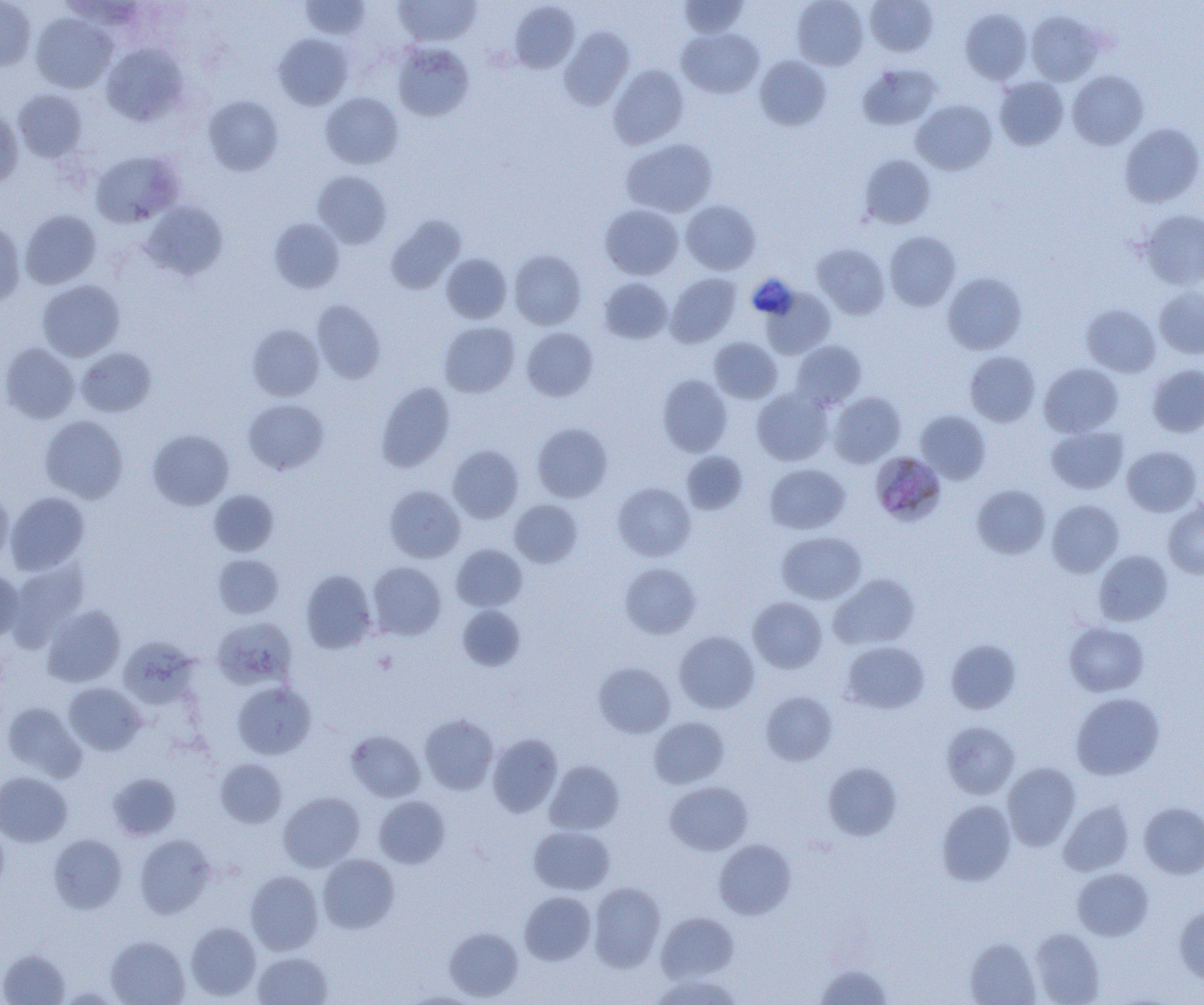
Summary:
  - Coordinate format: approximate bounding boxes as named x1/y1/x2/y2 corners in pixels
  - Uninfected red blood cell locations: (x1=299, y1=0, x2=371, y2=40), (x1=393, y1=0, x2=481, y2=46), (x1=792, y1=0, x2=868, y2=70), (x1=866, y1=0, x2=938, y2=56), (x1=0, y1=1, x2=36, y2=71), (x1=679, y1=1, x2=748, y2=38), (x1=509, y1=2, x2=580, y2=73), (x1=961, y1=8, x2=1032, y2=84), (x1=1025, y1=11, x2=1103, y2=85), (x1=31, y1=13, x2=116, y2=93), (x1=559, y1=27, x2=634, y2=110), (x1=677, y1=28, x2=764, y2=98), (x1=273, y1=33, x2=354, y2=110), (x1=392, y1=42, x2=474, y2=120), (x1=101, y1=44, x2=188, y2=126), (x1=754, y1=55, x2=831, y2=131), (x1=857, y1=63, x2=942, y2=130), (x1=608, y1=64, x2=688, y2=149), (x1=1067, y1=70, x2=1149, y2=149), (x1=994, y1=77, x2=1068, y2=150), (x1=13, y1=90, x2=88, y2=162), (x1=320, y1=92, x2=404, y2=169), (x1=203, y1=95, x2=283, y2=175), (x1=912, y1=99, x2=997, y2=175), (x1=0, y1=109, x2=23, y2=189), (x1=1119, y1=122, x2=1204, y2=207), (x1=622, y1=138, x2=717, y2=217), (x1=90, y1=150, x2=184, y2=227), (x1=859, y1=154, x2=936, y2=229), (x1=313, y1=170, x2=392, y2=248), (x1=681, y1=199, x2=760, y2=274), (x1=142, y1=200, x2=227, y2=280), (x1=600, y1=204, x2=683, y2=279), (x1=20, y1=210, x2=101, y2=289), (x1=1140, y1=210, x2=1204, y2=289), (x1=385, y1=215, x2=465, y2=294), (x1=269, y1=218, x2=344, y2=293), (x1=0, y1=219, x2=26, y2=307), (x1=884, y1=231, x2=961, y2=311), (x1=812, y1=243, x2=890, y2=319), (x1=509, y1=249, x2=586, y2=330), (x1=441, y1=254, x2=512, y2=324), (x1=942, y1=272, x2=1026, y2=354), (x1=665, y1=273, x2=741, y2=347), (x1=598, y1=278, x2=672, y2=344), (x1=37, y1=279, x2=125, y2=361), (x1=762, y1=287, x2=835, y2=359), (x1=1154, y1=287, x2=1204, y2=359), (x1=311, y1=300, x2=386, y2=383), (x1=1081, y1=303, x2=1160, y2=376), (x1=439, y1=321, x2=520, y2=397), (x1=247, y1=324, x2=324, y2=401), (x1=522, y1=328, x2=598, y2=400), (x1=709, y1=337, x2=782, y2=403), (x1=791, y1=340, x2=867, y2=410), (x1=0, y1=343, x2=80, y2=423), (x1=76, y1=347, x2=156, y2=417), (x1=965, y1=351, x2=1040, y2=426), (x1=1039, y1=363, x2=1123, y2=438), (x1=1146, y1=365, x2=1204, y2=437), (x1=656, y1=374, x2=733, y2=457), (x1=376, y1=382, x2=455, y2=472), (x1=752, y1=388, x2=833, y2=465), (x1=828, y1=392, x2=906, y2=468), (x1=243, y1=398, x2=329, y2=474), (x1=915, y1=410, x2=991, y2=485), (x1=39, y1=415, x2=128, y2=503), (x1=532, y1=422, x2=613, y2=502), (x1=1046, y1=426, x2=1128, y2=494), (x1=147, y1=428, x2=234, y2=510), (x1=448, y1=444, x2=524, y2=523), (x1=1121, y1=445, x2=1202, y2=516), (x1=681, y1=451, x2=748, y2=514), (x1=764, y1=464, x2=850, y2=534), (x1=612, y1=482, x2=696, y2=561), (x1=972, y1=484, x2=1050, y2=559), (x1=384, y1=486, x2=465, y2=563), (x1=0, y1=487, x2=13, y2=570), (x1=208, y1=489, x2=279, y2=556), (x1=5, y1=491, x2=89, y2=575), (x1=510, y1=499, x2=582, y2=568), (x1=1163, y1=499, x2=1204, y2=578), (x1=1046, y1=500, x2=1124, y2=577), (x1=777, y1=531, x2=867, y2=604), (x1=451, y1=544, x2=527, y2=611), (x1=1093, y1=550, x2=1173, y2=626), (x1=212, y1=554, x2=284, y2=619), (x1=7, y1=560, x2=90, y2=648), (x1=367, y1=562, x2=446, y2=640), (x1=619, y1=562, x2=701, y2=639), (x1=0, y1=569, x2=23, y2=644), (x1=300, y1=569, x2=377, y2=653), (x1=829, y1=573, x2=921, y2=650), (x1=748, y1=596, x2=827, y2=672), (x1=42, y1=604, x2=125, y2=687), (x1=457, y1=605, x2=525, y2=671), (x1=211, y1=617, x2=296, y2=690), (x1=1064, y1=622, x2=1149, y2=696), (x1=674, y1=631, x2=759, y2=714), (x1=120, y1=637, x2=200, y2=709), (x1=946, y1=639, x2=1021, y2=714), (x1=841, y1=641, x2=929, y2=713), (x1=594, y1=662, x2=675, y2=738), (x1=233, y1=682, x2=316, y2=759), (x1=63, y1=683, x2=146, y2=755), (x1=761, y1=691, x2=837, y2=765), (x1=1071, y1=692, x2=1165, y2=779), (x1=2, y1=702, x2=85, y2=781), (x1=420, y1=714, x2=498, y2=795), (x1=649, y1=717, x2=729, y2=788), (x1=942, y1=722, x2=1020, y2=798), (x1=346, y1=730, x2=426, y2=802), (x1=487, y1=733, x2=562, y2=817), (x1=215, y1=758, x2=287, y2=827), (x1=544, y1=760, x2=624, y2=834), (x1=823, y1=762, x2=903, y2=841), (x1=1002, y1=762, x2=1081, y2=851), (x1=0, y1=771, x2=72, y2=846), (x1=107, y1=773, x2=181, y2=840), (x1=665, y1=781, x2=753, y2=855), (x1=279, y1=791, x2=365, y2=871), (x1=373, y1=796, x2=450, y2=868), (x1=936, y1=800, x2=1016, y2=886), (x1=1058, y1=801, x2=1134, y2=876), (x1=1139, y1=802, x2=1204, y2=878), (x1=529, y1=826, x2=615, y2=895), (x1=49, y1=833, x2=126, y2=914), (x1=134, y1=834, x2=216, y2=918), (x1=714, y1=839, x2=796, y2=919), (x1=318, y1=854, x2=400, y2=933), (x1=1072, y1=868, x2=1153, y2=940), (x1=245, y1=870, x2=323, y2=955), (x1=588, y1=882, x2=665, y2=972), (x1=520, y1=891, x2=596, y2=965), (x1=1174, y1=905, x2=1204, y2=985), (x1=656, y1=912, x2=739, y2=982), (x1=185, y1=922, x2=261, y2=1001), (x1=444, y1=927, x2=523, y2=1002), (x1=1030, y1=928, x2=1105, y2=1005), (x1=106, y1=936, x2=189, y2=1005), (x1=965, y1=937, x2=1040, y2=1005), (x1=0, y1=949, x2=70, y2=1005), (x1=253, y1=952, x2=333, y2=1005), (x1=815, y1=963, x2=893, y2=1005), (x1=651, y1=974, x2=743, y2=1005)
  - Platelet locations: (x1=747, y1=275, x2=798, y2=320)
  - Plasmodium malariae-infected red blood cell locations: (x1=869, y1=459, x2=952, y2=527)
  - Slide-level diagnosis: Plasmodium malariae
  - Magnification: 1000x
  - Modality: optical microscopy
  - Image size: 1204×1005 pixels
  - Field of view: single
  - Preparation: thin blood smear